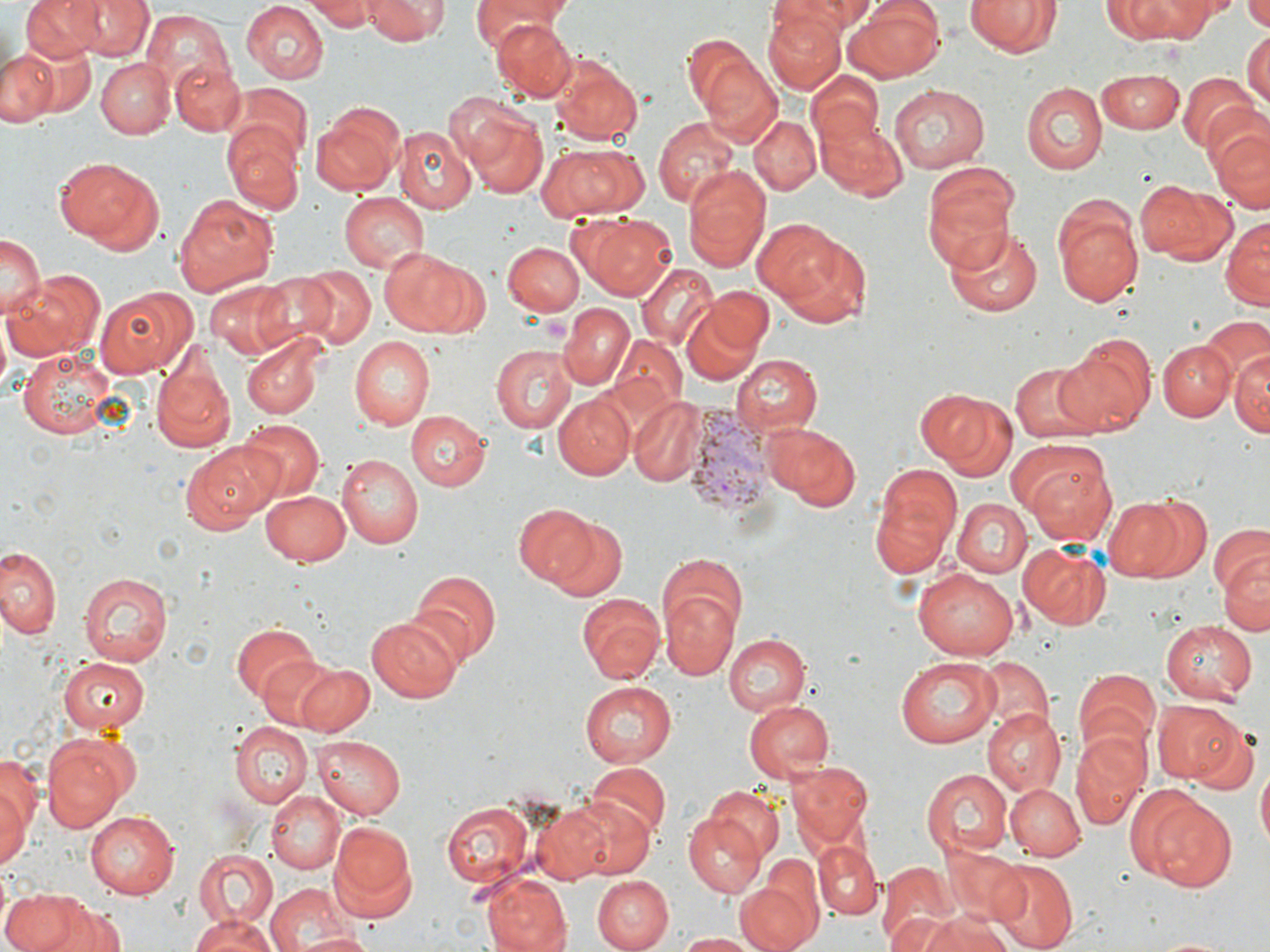 Approximate bounding boxes as [x1, y1, x2, y2] in pixels. Plasmodium vivax-infected red blood cell locations: [690, 402, 773, 519]. Uninfected red blood cell locations: [66, 0, 152, 60], [307, 0, 378, 30], [366, 0, 447, 45], [472, 0, 568, 49], [769, 0, 879, 34], [844, 0, 946, 82], [962, 0, 1063, 59], [24, 1, 101, 61], [242, 1, 330, 84], [1117, 2, 1218, 40], [1241, 2, 1270, 30], [140, 10, 232, 93], [763, 11, 843, 94], [489, 18, 576, 100], [1242, 31, 1268, 108], [11, 33, 96, 121], [0, 46, 57, 129], [551, 56, 643, 145], [700, 56, 782, 148], [97, 58, 174, 138], [171, 62, 244, 137], [808, 69, 887, 151], [1095, 69, 1185, 131], [1177, 73, 1259, 156], [233, 83, 312, 164], [1022, 83, 1105, 174], [890, 84, 990, 172], [459, 106, 549, 198], [311, 107, 404, 196], [750, 112, 821, 195], [651, 116, 742, 210], [815, 117, 907, 198], [1206, 119, 1270, 210], [222, 124, 304, 216], [395, 125, 475, 213], [536, 143, 647, 219], [58, 157, 163, 254], [920, 160, 1021, 271], [681, 165, 771, 275], [1134, 179, 1236, 264], [171, 192, 277, 297], [339, 192, 430, 271], [1054, 199, 1145, 307], [570, 213, 678, 298], [1222, 218, 1269, 310], [762, 224, 871, 328], [941, 225, 1043, 321], [0, 233, 43, 319], [504, 241, 585, 315], [379, 246, 472, 337], [634, 263, 717, 350], [297, 266, 377, 350], [12, 271, 106, 362], [248, 272, 336, 350], [204, 278, 294, 357], [96, 283, 200, 379], [699, 284, 775, 359], [679, 301, 768, 387], [557, 302, 634, 390], [1181, 319, 1262, 410], [241, 334, 328, 419], [349, 336, 435, 430], [610, 336, 687, 417], [1053, 336, 1154, 437], [1158, 340, 1235, 420], [490, 343, 576, 432], [149, 345, 236, 454], [1230, 346, 1269, 440], [17, 347, 118, 439], [732, 355, 822, 436], [1009, 362, 1099, 442], [930, 390, 1017, 480], [554, 394, 633, 480], [627, 396, 706, 485], [406, 410, 490, 491], [236, 418, 326, 501], [761, 421, 862, 512], [180, 444, 272, 535], [339, 452, 426, 546], [1023, 456, 1117, 547], [868, 462, 962, 579], [259, 490, 352, 568], [1105, 493, 1213, 581], [951, 497, 1031, 577], [514, 503, 602, 586], [549, 518, 628, 602], [1208, 524, 1268, 601], [1019, 542, 1112, 631], [0, 545, 63, 642], [1218, 553, 1269, 638], [657, 558, 746, 676], [913, 566, 1018, 660], [407, 569, 500, 666], [78, 570, 174, 665], [66, 581, 162, 731], [576, 593, 666, 684], [365, 616, 463, 702], [1161, 620, 1256, 702], [229, 621, 319, 704], [723, 632, 810, 716], [252, 651, 346, 731], [56, 655, 151, 735], [895, 656, 1001, 746], [976, 656, 1051, 732], [287, 660, 375, 734], [1074, 666, 1159, 755], [578, 680, 677, 767], [1152, 699, 1244, 784], [742, 700, 833, 783], [981, 709, 1065, 795], [231, 721, 312, 808], [1187, 721, 1261, 798], [1069, 729, 1151, 828], [40, 732, 136, 834], [313, 734, 403, 818], [0, 750, 41, 853], [787, 761, 876, 849], [1256, 761, 1270, 852], [585, 763, 669, 841], [921, 768, 1013, 859], [0, 777, 29, 874], [1004, 781, 1085, 861], [707, 787, 785, 861], [1129, 787, 1238, 894], [266, 792, 344, 873], [562, 795, 656, 881], [530, 800, 622, 884], [440, 801, 534, 890], [85, 810, 179, 900], [682, 811, 766, 898], [331, 820, 417, 914], [814, 842, 881, 920], [194, 848, 278, 932], [986, 860, 1079, 949], [876, 861, 957, 947], [737, 869, 822, 952], [483, 874, 570, 952], [589, 875, 671, 951], [264, 881, 356, 952], [1, 888, 103, 952], [47, 899, 127, 952], [910, 909, 1019, 952], [188, 913, 280, 952], [291, 931, 376, 952], [676, 932, 766, 951]. Slide-level diagnosis: Plasmodium vivax. 1000x magnification. Image is 1270×952 pixels. Thin blood smear. One field of a larger specimen. May-Grünwald-Giemsa-stained preparation. Optical microscopy.